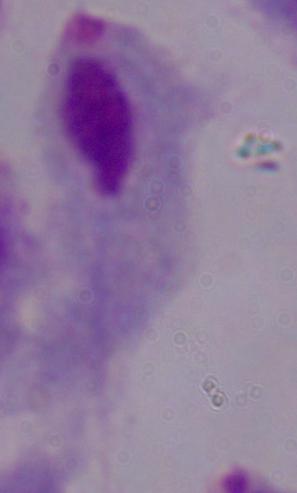

identification: trichomonad
modality: micrograph
magnification: 1000x